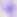

{
  "magnification": "400x",
  "identification": "Toxoplasma gondii",
  "modality": "micrograph"
}